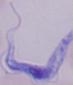

Summary:
  - Modality: micrograph
  - Magnification: 1000x
  - Identification: trypanosome